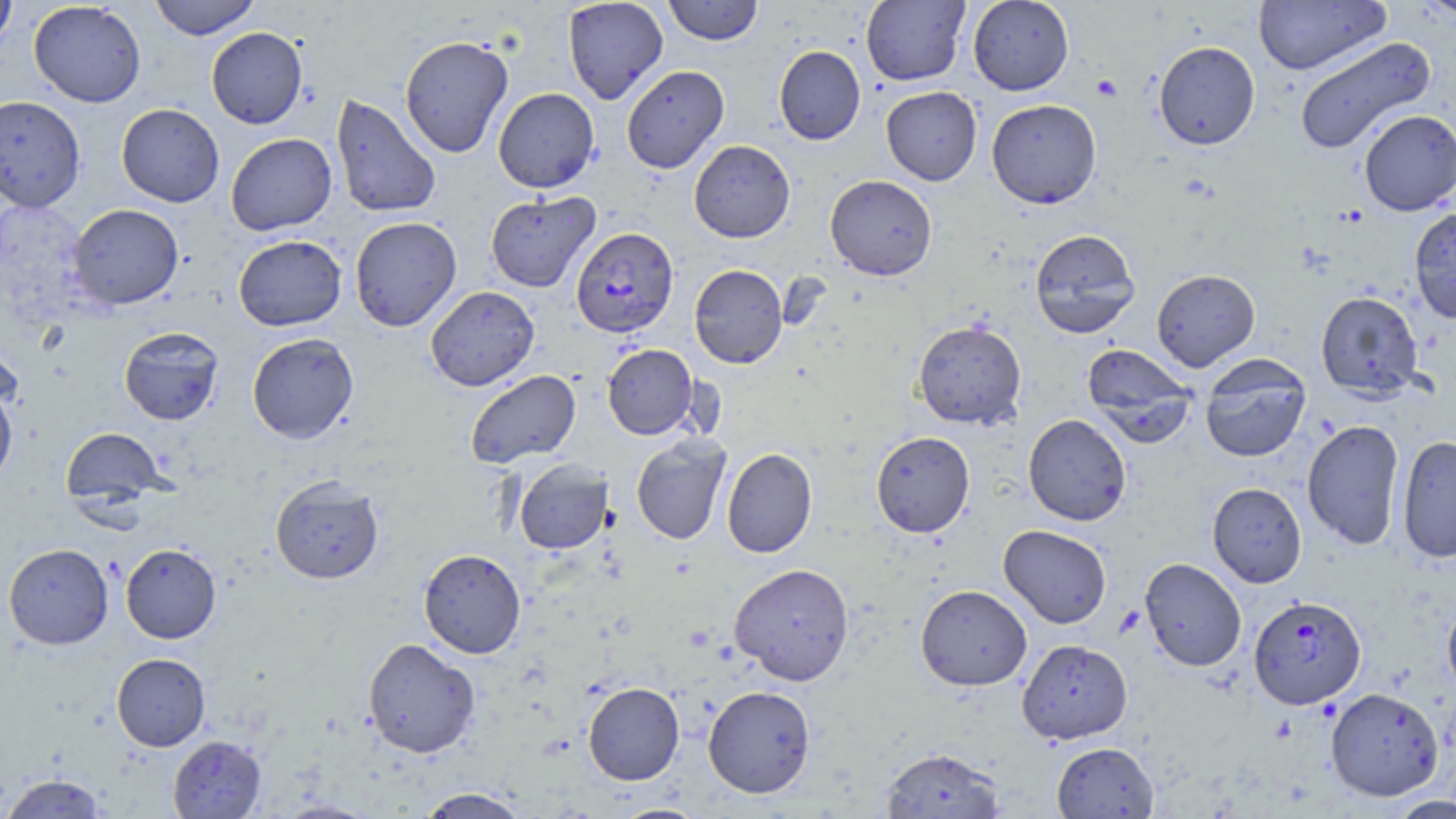

slide-level diagnosis = Plasmodium falciparum
platelet locations = approximate bounding boxes as [x1, y1, x2, y2] in pixels: [1092, 74, 1122, 101]
stain = May-Grünwald-Giemsa
Plasmodium falciparum-infected red blood cell locations = approximate bounding boxes as [x1, y1, x2, y2] in pixels: [571, 227, 678, 339], [1249, 594, 1366, 710]
preparation = thin blood film
uninfected red blood cell locations = approximate bounding boxes as [x1, y1, x2, y2] in pixels: [0, 0, 18, 52], [149, 0, 261, 40], [563, 0, 668, 105], [663, 0, 764, 45], [861, 0, 970, 86], [968, 0, 1074, 95], [1253, 0, 1391, 75], [1416, 0, 1456, 20], [29, 1, 146, 107], [206, 27, 308, 129], [399, 35, 514, 157], [1293, 36, 1435, 155], [1153, 41, 1260, 150], [774, 45, 866, 145], [621, 65, 729, 173], [881, 86, 982, 185], [493, 88, 599, 193], [331, 94, 442, 219], [0, 95, 86, 213], [986, 99, 1102, 209], [116, 103, 224, 207], [1358, 109, 1456, 216], [226, 133, 337, 235], [689, 140, 795, 243], [825, 174, 938, 281], [485, 192, 600, 292], [68, 203, 184, 309], [1408, 206, 1456, 324], [349, 216, 462, 331], [1029, 229, 1140, 339], [233, 235, 347, 331], [689, 264, 788, 369], [1151, 269, 1261, 371], [425, 286, 539, 390], [1315, 291, 1424, 400], [912, 319, 1027, 430], [119, 326, 224, 425], [247, 332, 359, 444], [602, 344, 699, 440], [1082, 344, 1197, 444], [1199, 357, 1311, 462], [465, 370, 581, 468], [0, 383, 18, 487], [1023, 413, 1131, 526], [1302, 419, 1405, 550], [60, 426, 169, 509], [871, 431, 975, 537], [1396, 435, 1456, 563], [631, 436, 731, 545], [721, 448, 817, 558], [513, 459, 613, 554], [269, 475, 384, 584], [1207, 482, 1307, 587], [998, 525, 1112, 628], [3, 543, 114, 649], [120, 543, 222, 643], [419, 549, 526, 658], [1140, 557, 1247, 672], [729, 563, 855, 686], [916, 584, 1032, 690], [1442, 595, 1456, 697], [362, 637, 481, 758], [1016, 638, 1133, 744], [111, 653, 211, 750], [583, 682, 684, 785], [703, 685, 816, 798], [1325, 687, 1444, 801], [168, 735, 266, 818], [1052, 742, 1159, 818], [880, 746, 1006, 819], [1, 773, 109, 818], [416, 787, 531, 818], [1385, 795, 1456, 819], [610, 804, 709, 819]
magnification = 1000x
image size = 1456×819 pixels
modality = optical microscopy
field of view = single